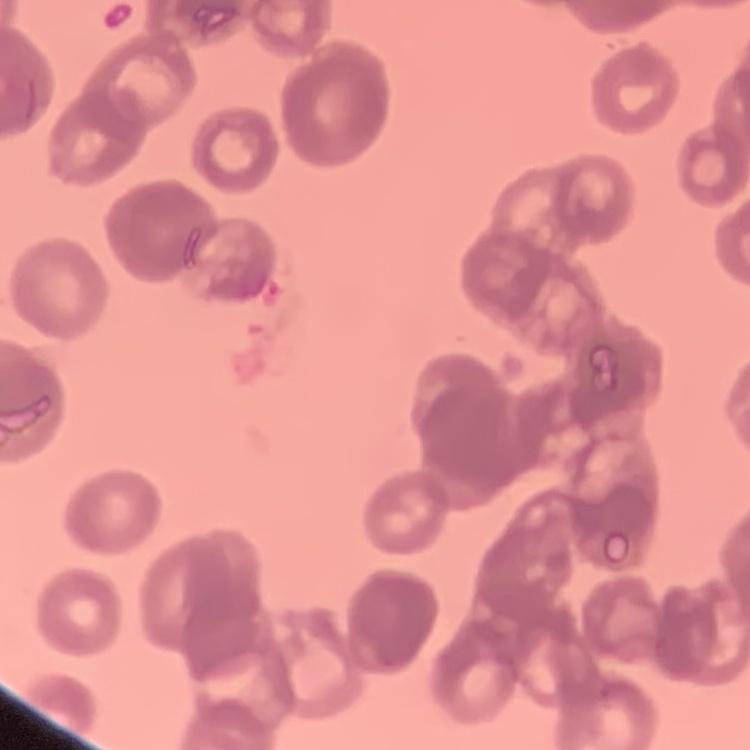
Summary:
  - Erythrocyte morphology: rouleaux formation
  - Preparation: thin peripheral smear
  - Stain: Field's or Giemsa
  - Image type: square crop of a larger photomicrograph